Classify this cell by malaria status.
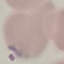

Parasitized.

Thin blood film. Cell patch, automatically extracted from a larger field of view and resized to 64 × 64 pixels. Acquired by smartphone through the microscope eyepiece. Giemsa stain.